State which parasite is depicted.
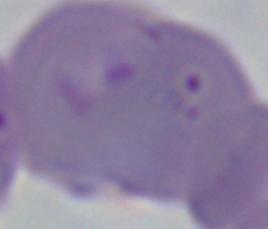

This is Babesia.

Summary:
  - Modality: photomicrograph
  - Magnification: 1000x